Outline each Plasmodium ovale-infected red blood cell.
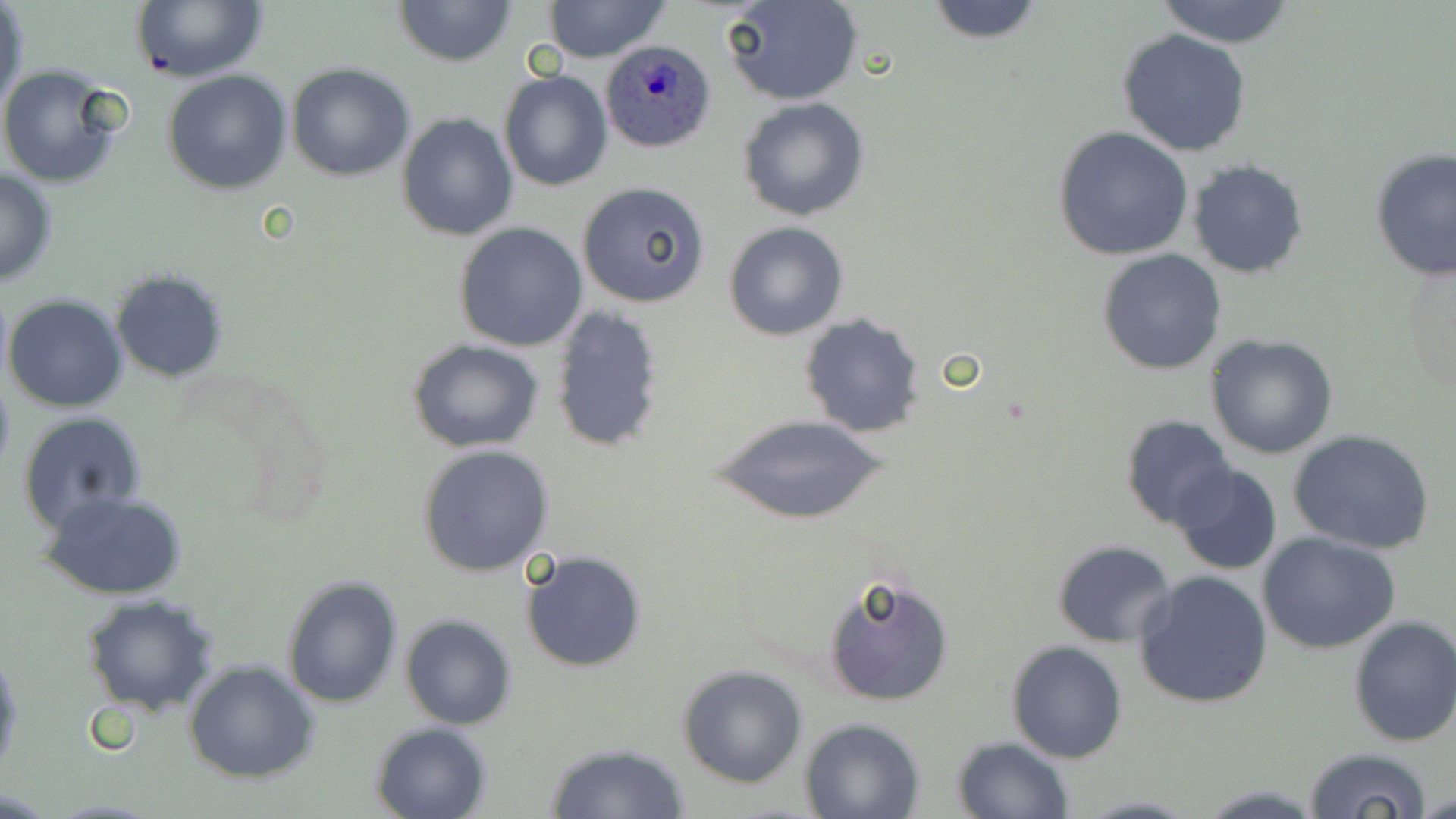

Approximate bounding boxes as (x1,y1)-(x2,y2) corner pairs in pixels.
Plasmodium ovale-infected red blood cells: (599,40)-(716,153).

Summary:
  - Uninfected red blood cell locations: (393,0)-(516,67), (721,0)-(863,106), (923,0)-(1047,45), (131,1)-(268,83), (543,1)-(671,63), (1152,1)-(1298,47), (1,4)-(28,119), (1119,28)-(1251,156), (0,63)-(130,191), (287,63)-(415,182), (163,70)-(292,193), (498,71)-(612,191), (737,97)-(869,221), (397,112)-(518,243), (1052,127)-(1195,262), (1370,148)-(1456,281), (1188,160)-(1309,278), (0,166)-(58,286), (576,182)-(708,307), (723,220)-(849,340), (455,223)-(587,351), (1097,249)-(1226,376), (1403,254)-(1455,398), (109,267)-(230,383), (4,294)-(128,411), (549,307)-(667,453), (798,312)-(927,439), (1206,334)-(1338,460), (406,339)-(546,454), (18,412)-(148,537), (713,413)-(889,527), (1121,415)-(1234,528), (1287,428)-(1436,555), (417,445)-(555,578), (1172,464)-(1283,577), (40,490)-(189,601), (1257,531)-(1400,654), (1051,539)-(1178,646), (520,550)-(647,673), (1133,569)-(1276,710), (822,571)-(954,707), (281,574)-(403,709), (80,595)-(221,718), (400,614)-(518,730), (1348,616)-(1456,748), (1006,640)-(1129,763), (0,649)-(22,776), (184,661)-(319,784), (678,666)-(806,787), (799,717)-(924,819), (370,722)-(492,819), (952,737)-(1073,819), (544,743)-(691,818), (1305,746)-(1433,819), (1192,784)-(1330,817), (1420,789)-(1456,817)
  - Slide-level diagnosis: Plasmodium ovale
  - Image size: 1456×819 pixels
  - Magnification: 1000x
  - Modality: optical microscopy
  - Field of view: single
  - Stain: May-Grünwald-Giemsa
  - Preparation: thin blood smear